State which parasite is depicted.
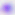
Toxoplasma gondii.

Summary:
  - Magnification: 400x
  - Modality: photomicrograph